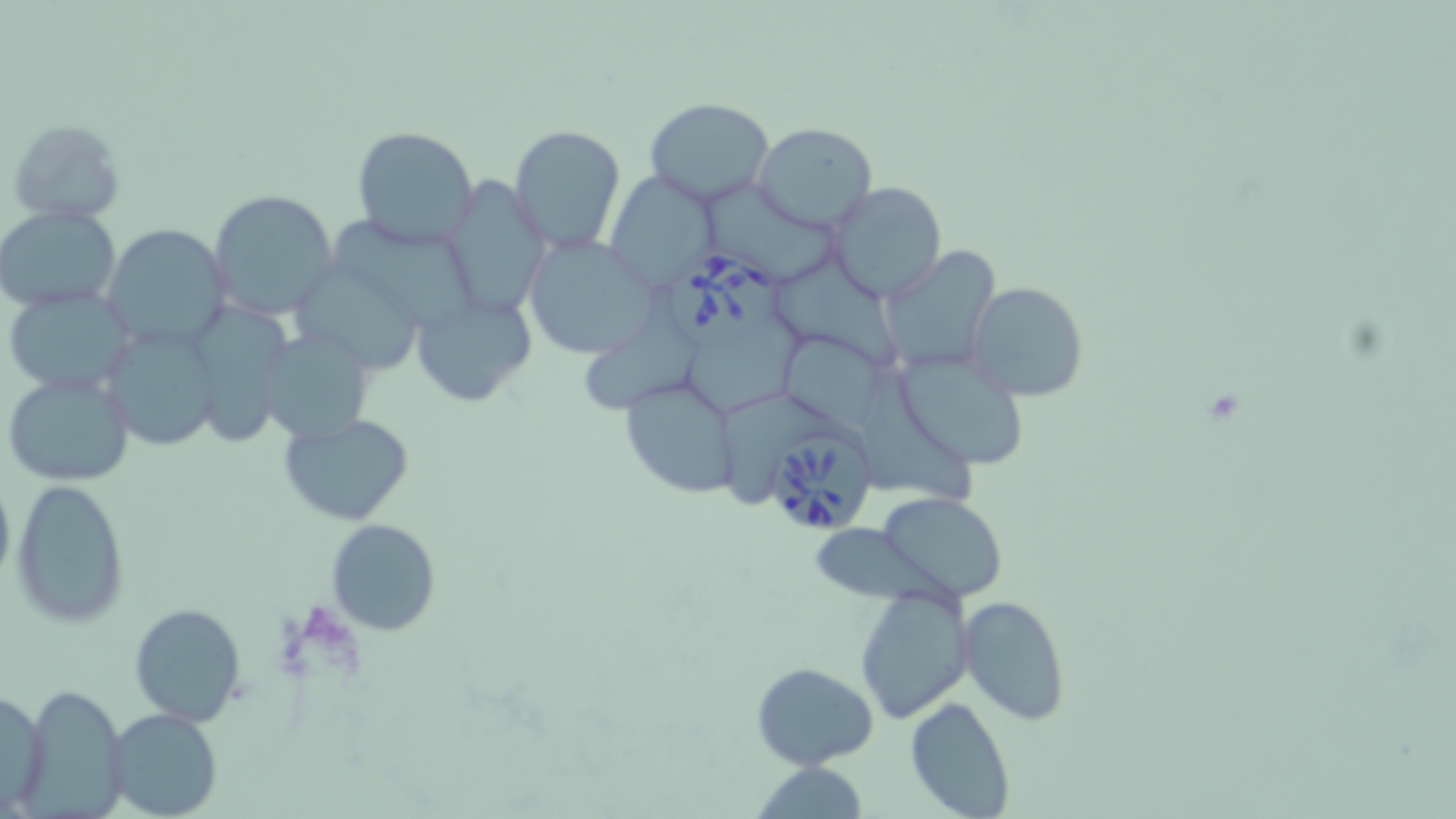
Summary:
  - Coordinate format: approximate bounding boxes as named x1/y1/x2/y2 corners in pixels
  - Babesia divergens-infected red blood cell locations: (x1=669, y1=247, x2=786, y2=354), (x1=767, y1=423, x2=880, y2=537)
  - Uninfected red blood cell locations: (x1=644, y1=97, x2=775, y2=208), (x1=6, y1=119, x2=124, y2=224), (x1=752, y1=122, x2=877, y2=232), (x1=509, y1=125, x2=626, y2=255), (x1=351, y1=126, x2=480, y2=248), (x1=607, y1=170, x2=722, y2=291), (x1=441, y1=175, x2=550, y2=323), (x1=706, y1=176, x2=846, y2=286), (x1=826, y1=181, x2=948, y2=302), (x1=208, y1=190, x2=341, y2=324), (x1=0, y1=205, x2=122, y2=312), (x1=335, y1=213, x2=481, y2=334), (x1=100, y1=223, x2=228, y2=349), (x1=520, y1=234, x2=660, y2=360), (x1=879, y1=244, x2=999, y2=374), (x1=778, y1=254, x2=909, y2=369), (x1=300, y1=268, x2=426, y2=374), (x1=966, y1=280, x2=1089, y2=402), (x1=586, y1=286, x2=701, y2=416), (x1=3, y1=287, x2=139, y2=398), (x1=412, y1=292, x2=536, y2=407), (x1=197, y1=301, x2=300, y2=452), (x1=101, y1=322, x2=225, y2=452), (x1=686, y1=325, x2=813, y2=411), (x1=257, y1=327, x2=376, y2=444), (x1=776, y1=329, x2=890, y2=430), (x1=895, y1=348, x2=1033, y2=470), (x1=2, y1=369, x2=136, y2=488), (x1=620, y1=372, x2=740, y2=499), (x1=866, y1=376, x2=984, y2=513), (x1=720, y1=391, x2=831, y2=497), (x1=280, y1=412, x2=414, y2=525), (x1=0, y1=464, x2=15, y2=600), (x1=11, y1=477, x2=131, y2=626), (x1=878, y1=492, x2=1007, y2=603), (x1=325, y1=519, x2=443, y2=636), (x1=807, y1=522, x2=971, y2=620), (x1=856, y1=585, x2=971, y2=723), (x1=958, y1=594, x2=1070, y2=726), (x1=130, y1=602, x2=247, y2=727), (x1=752, y1=661, x2=878, y2=769), (x1=21, y1=684, x2=126, y2=815), (x1=0, y1=685, x2=49, y2=813), (x1=904, y1=696, x2=1017, y2=819), (x1=106, y1=709, x2=224, y2=819), (x1=748, y1=761, x2=873, y2=818)
  - Slide-level diagnosis: Babesia divergens
  - Image size: 1456×819 pixels
  - Field of view: one of a larger specimen
  - Preparation: thin blood film
  - Magnification: 1000x
  - Stain: May-Grünwald-Giemsa
  - Modality: light microscopy